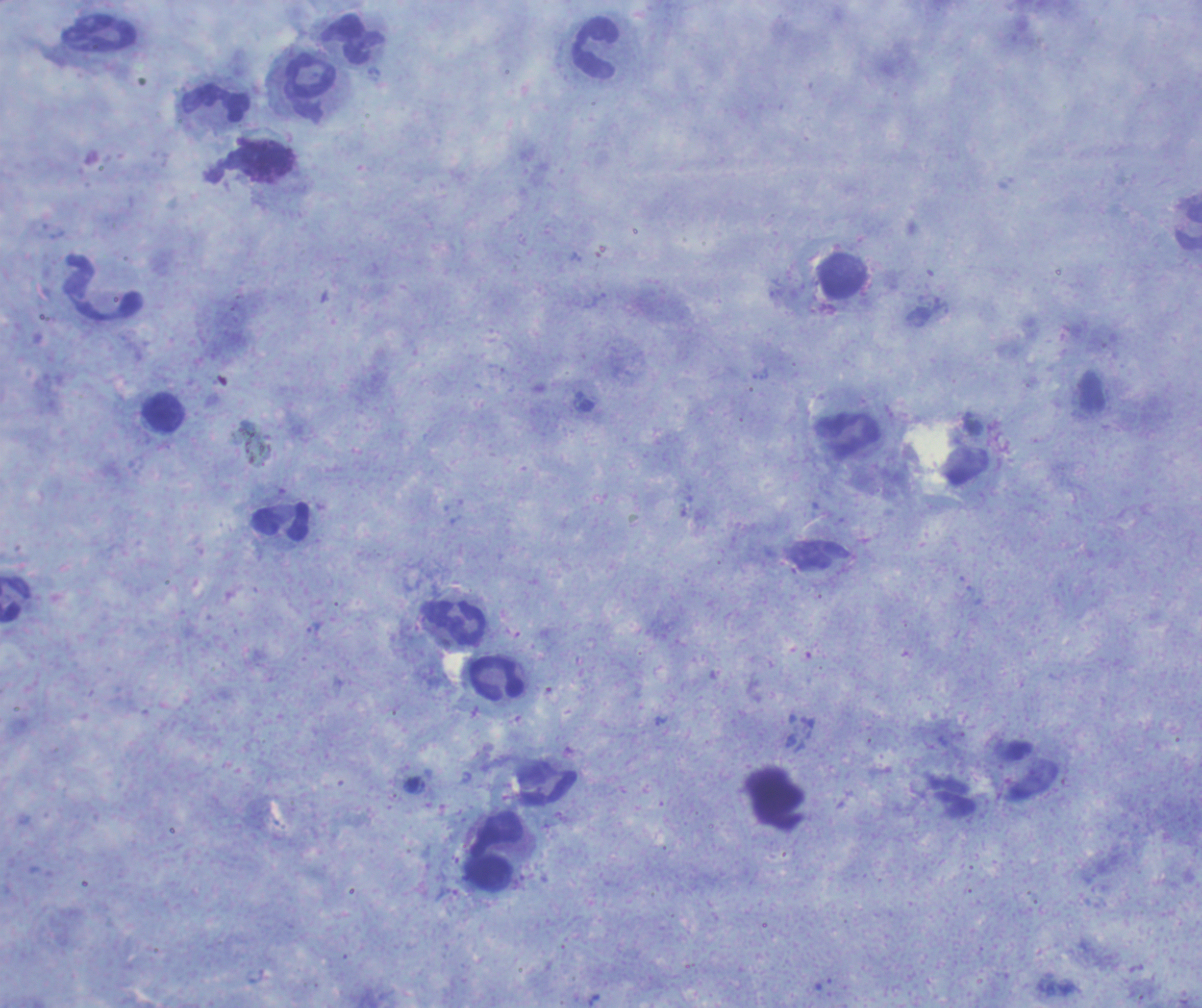

coordinate format = approximate object centers, in pixels from the top-left corner
leukocyte locations = (x=99, y=34), (x=354, y=40), (x=595, y=50), (x=310, y=76), (x=216, y=102), (x=1189, y=227), (x=842, y=285), (x=104, y=288), (x=164, y=412), (x=847, y=437), (x=281, y=521), (x=16, y=600), (x=453, y=623), (x=497, y=678), (x=548, y=788), (x=495, y=851)
background quality = satisfactory
magnification = 100x
coloration quality = good
stain = Romanowsky
field of view = single
preparation = thick smear of blood
context = previously used in a real diagnosis
image size = 1202×1008 pixels
result = no malaria parasites seen